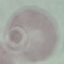
Summary:
  - Malaria status: uninfected
  - Capture: smartphone through the microscope eyepiece
  - Image type: automatically extracted cell patch, resized to 64 × 64 pixels
  - Stain: Giemsa
  - Preparation: thin smear